State which parasite is depicted.
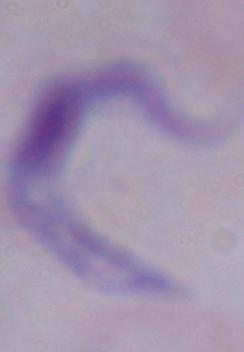
This is a trypanosome.

Photomicrograph. 1000x magnification.